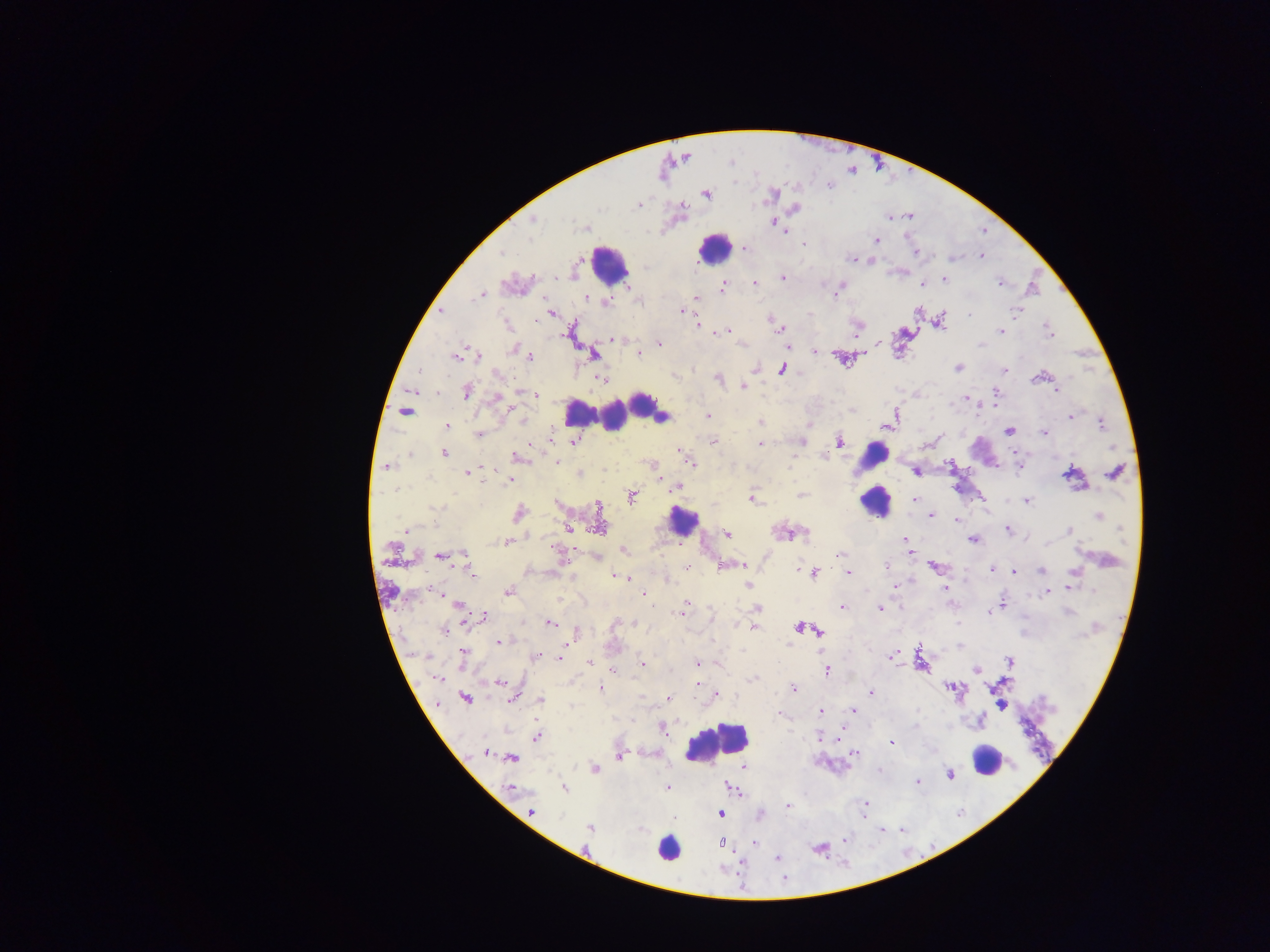

Approximate centers as [x, y] in pixels.
Summary:
  - Leukocyte locations: [714, 247], [608, 265], [644, 405], [619, 409], [599, 413], [581, 414], [659, 416], [873, 455], [876, 501], [683, 521], [717, 742], [986, 761], [666, 848]
  - Malaria parasite locations: [706, 193], [639, 204], [682, 205], [793, 208], [909, 216], [890, 217], [773, 221], [585, 227], [783, 232], [876, 241], [804, 242], [743, 248], [915, 252], [980, 256], [853, 259], [869, 259], [782, 278], [942, 279], [1000, 282], [755, 283], [921, 284], [722, 287], [838, 289], [481, 294], [585, 297], [696, 299], [607, 301], [442, 311], [680, 311], [1017, 311], [551, 313], [940, 321], [696, 324], [779, 328], [856, 329], [727, 330], [1001, 330], [1049, 335], [613, 339], [658, 343], [877, 344], [788, 345], [513, 349], [815, 352], [593, 353], [638, 353], [475, 354], [459, 355], [528, 356], [842, 358], [757, 368], [782, 368], [958, 368], [1004, 371], [1042, 375], [602, 378], [717, 378], [743, 386], [1056, 391], [466, 392], [994, 392], [535, 394], [496, 397], [965, 399], [996, 406], [510, 408], [405, 411], [707, 415], [1071, 415], [895, 416], [522, 422], [760, 423], [889, 423], [1101, 423], [447, 425], [1009, 431], [1044, 432], [478, 434], [713, 440], [574, 441], [838, 442], [759, 443], [798, 443], [681, 451], [444, 453], [516, 458], [690, 461], [557, 462], [652, 463], [1019, 465], [387, 466], [466, 471], [916, 471], [1115, 472], [580, 473], [1072, 475], [511, 479], [662, 479], [679, 486], [801, 494], [631, 495], [981, 496], [752, 497], [915, 499], [1026, 501], [519, 513], [932, 515], [1098, 516], [956, 520], [598, 526], [568, 527], [407, 529], [1008, 530], [1069, 531], [725, 533], [788, 533], [904, 538], [972, 539], [507, 542], [907, 545], [907, 550], [623, 551], [841, 553], [440, 555], [560, 555], [598, 558], [721, 565], [743, 565], [934, 565], [885, 566], [686, 567], [467, 569], [991, 569], [1041, 571], [814, 572], [848, 572], [1012, 572], [616, 576], [623, 576], [631, 579], [748, 585], [894, 585], [1069, 587], [946, 589], [509, 591], [441, 592], [1046, 592], [643, 593], [1003, 604], [685, 605], [460, 606], [842, 606], [757, 608], [682, 609], [879, 609], [988, 613], [482, 618], [550, 623], [799, 627], [753, 628], [445, 629], [818, 630], [574, 634], [499, 642], [891, 656], [462, 657], [536, 657], [559, 657], [920, 658], [1009, 660], [588, 663], [697, 663], [642, 664], [977, 669], [613, 670], [827, 670], [435, 677], [754, 678], [500, 681], [697, 684], [948, 687], [600, 688], [792, 688], [870, 694], [715, 695], [465, 697], [513, 697], [669, 697], [540, 700], [436, 703], [1000, 704], [853, 709], [820, 711], [661, 726], [844, 728], [537, 736], [819, 738], [891, 741], [487, 752], [855, 752], [619, 756], [509, 757], [511, 758], [743, 766], [594, 769], [949, 774], [917, 781], [511, 787], [563, 787], [667, 787], [729, 787], [865, 804], [788, 806], [530, 811], [719, 813], [673, 819], [590, 827], [882, 829], [722, 842], [755, 842], [776, 858]
  - Preparation: thick blood smear
  - Country: Ghana
  - Image size: 1270×952 pixels
  - Capture: mobile-phone photograph through a microscope
  - Field of view: single